Identify the cell.
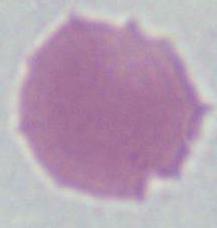

An erythrocyte.

Summary:
  - Modality: photomicrograph
  - Magnification: 1000x